Assess this cell for malaria.
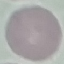

Uninfected.

Photographed with a smartphone camera at the microscope eyepiece. Thin smear of blood. Automatically extracted cell patch, resized to 64 × 64 pixels. Giemsa-stained preparation.